Classify this cell by malaria status.
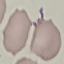
It is uninfected.

Summary:
  - Image type: automatically extracted cell patch, resized to 64 × 64 pixels
  - Capture: smartphone camera at the microscope eyepiece
  - Stain: Giemsa
  - Preparation: thin blood smear